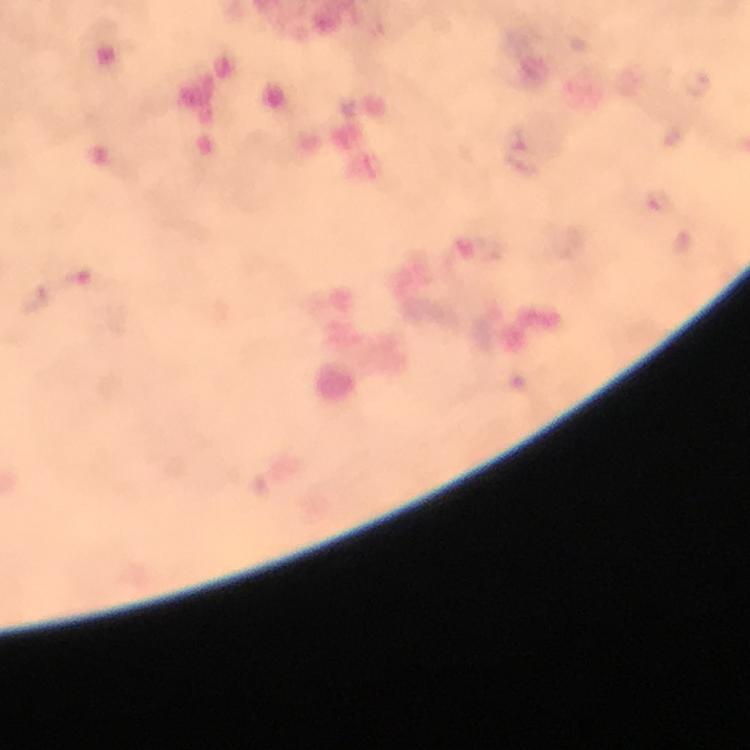

Approximate centers as {x, y} in pixels. Malaria parasite locations: {697, 83}, {523, 148}, {658, 201}, {87, 281}, {36, 300}. Photographed through the microscope with a smartphone camera. 100x magnification. A crop from one field of view. Giemsa stain. Immersion oil applied. From a diagnostic examination for malaria. Thick smear. Image is 750×750 pixels.